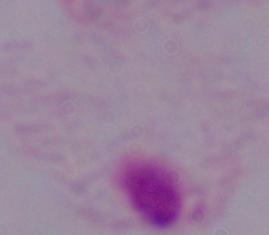
{
  "modality": "micrograph",
  "magnification": "1000x",
  "identification": "trichomonad"
}